Give the extent of all Plasmodium ovale-infected red blood cells.
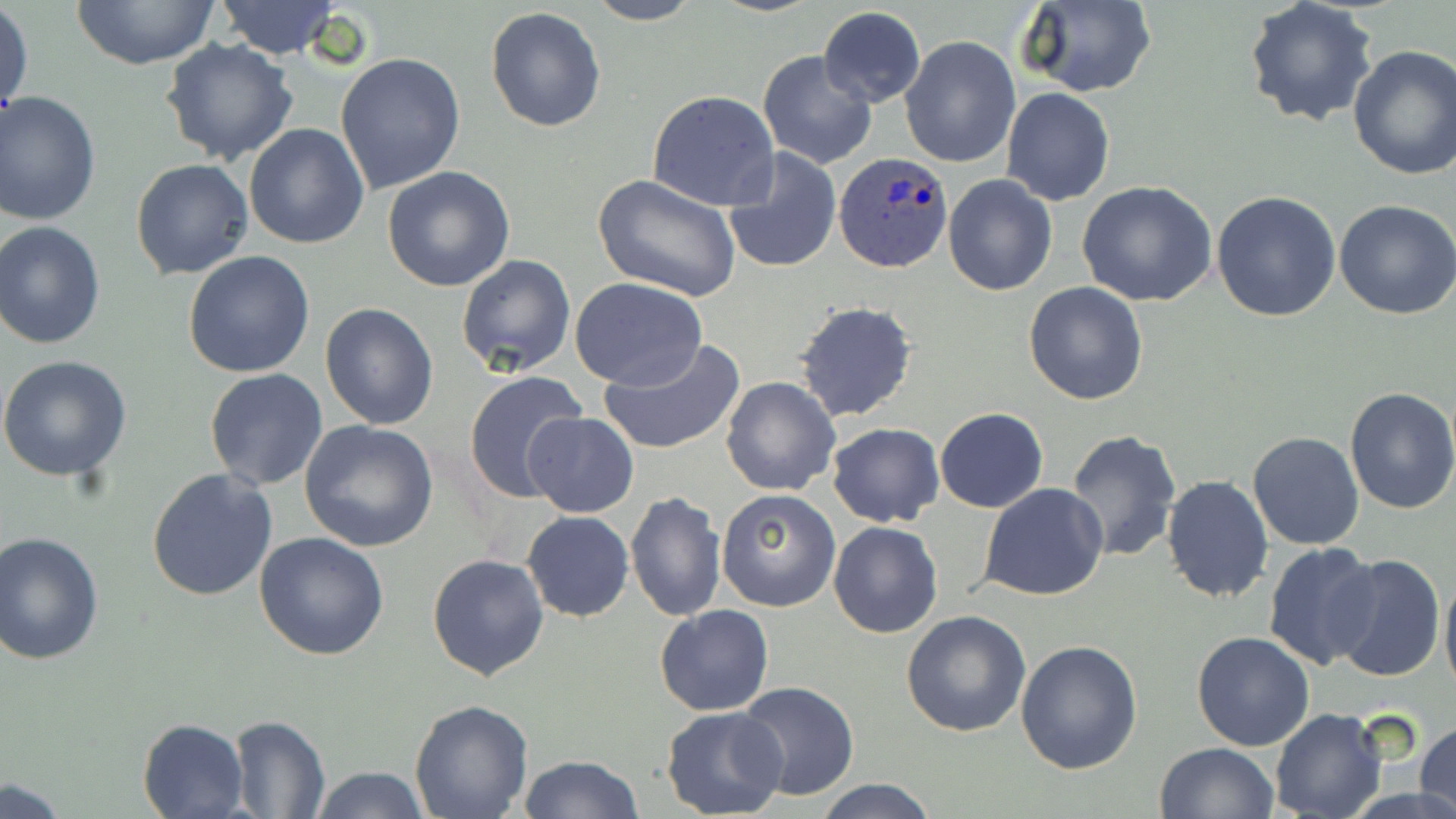

Approximate bounding boxes as (x1,y1)-(x2,y2) corner pairs in pixels.
Plasmodium ovale-infected red blood cells: (834,152)-(954,273).

slide-level diagnosis = Plasmodium ovale
magnification = 1000x
preparation = thin blood film
uninfected red blood cell locations = approximate bounding boxes as (x1,y1)-(x2,y2) corner pairs in pixels: (67,0)-(220,69), (213,1)-(343,59), (582,1)-(705,25), (1016,1)-(1157,98), (1243,1)-(1378,129), (1,4)-(34,123), (485,5)-(607,133), (818,7)-(926,108), (898,36)-(1019,169), (160,38)-(301,169), (1346,46)-(1456,180), (757,49)-(877,170), (335,53)-(466,196), (1002,89)-(1115,206), (645,91)-(779,211), (0,92)-(101,225), (242,122)-(369,250), (722,148)-(842,275), (130,158)-(253,279), (382,165)-(515,292), (593,174)-(740,301), (942,174)-(1059,295), (1076,179)-(1217,306), (1212,191)-(1343,323), (1334,199)-(1456,319), (0,221)-(108,351), (183,250)-(315,377), (456,253)-(577,377), (569,276)-(707,389), (1023,281)-(1150,404), (793,301)-(919,424), (319,302)-(440,431), (598,338)-(746,455), (0,354)-(132,483), (204,369)-(328,491), (463,371)-(589,505), (720,377)-(840,497), (1342,386)-(1456,516), (933,408)-(1049,512), (523,412)-(639,518), (298,419)-(441,553), (827,422)-(943,527), (1065,429)-(1181,561), (1248,431)-(1364,550), (146,467)-(278,599), (1160,474)-(1275,603), (980,483)-(1109,601), (715,488)-(839,611), (626,492)-(725,622), (522,511)-(634,623), (828,520)-(943,638), (0,530)-(105,666), (255,532)-(389,661), (1263,540)-(1381,670), (427,553)-(548,682), (1331,554)-(1445,685), (1439,563)-(1456,703), (654,604)-(774,717), (902,609)-(1032,737), (1191,632)-(1315,751), (1016,638)-(1144,775), (734,681)-(861,801), (408,698)-(534,818), (660,705)-(788,819), (1269,709)-(1388,819), (227,715)-(331,818), (137,717)-(250,817), (1416,720)-(1456,819), (1155,742)-(1278,819), (517,755)-(643,819), (309,765)-(431,819), (814,778)-(942,818), (0,779)-(72,818)
image size = 1456×819 pixels
modality = light microscopy
field of view = one of a larger specimen
stain = May-Grünwald-Giemsa